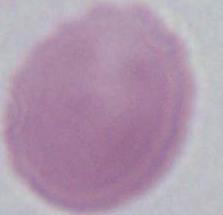

Photomicrograph. A red blood cell is seen. Captured at 1000x magnification.